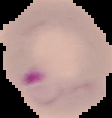

Summary:
  - Image type: segmented cell region with the area outside set to black
  - Malaria status: parasitized
  - Preparation: thin blood film
  - Image size: 112×118 pixels